Report the malaria status of this cell.
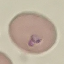
It is parasitized.

capture = smartphone through the microscope eyepiece
stain = Giemsa
image type = cell patch, automatically extracted from a larger field of view and resized to 64 × 64 pixels
preparation = thin smear